Describe the morphology of the erythrocytes.
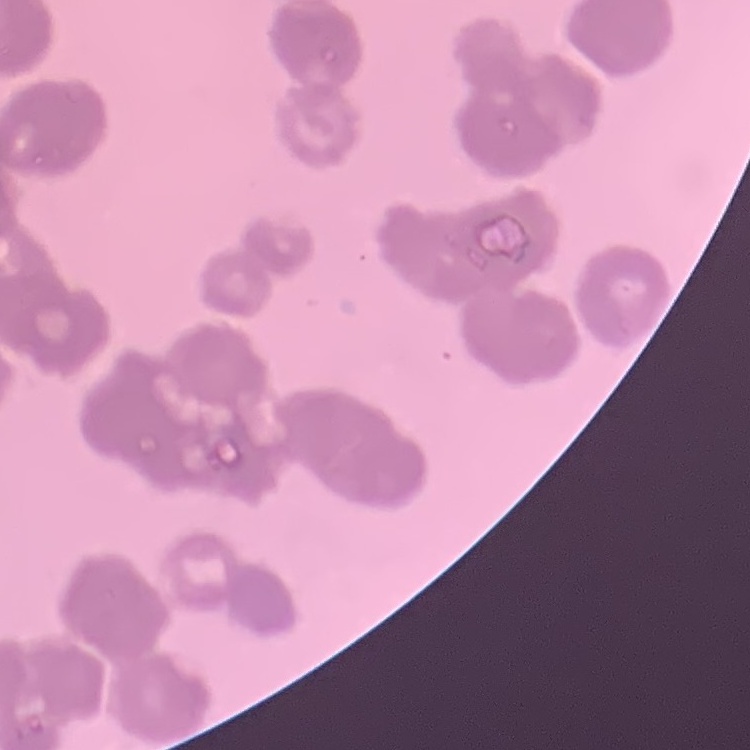
They show rouleaux formation.

Summary:
  - Image type: one tile cut from a larger photomicrograph
  - Preparation: thin blood film
  - Stain: Field's or Giemsa